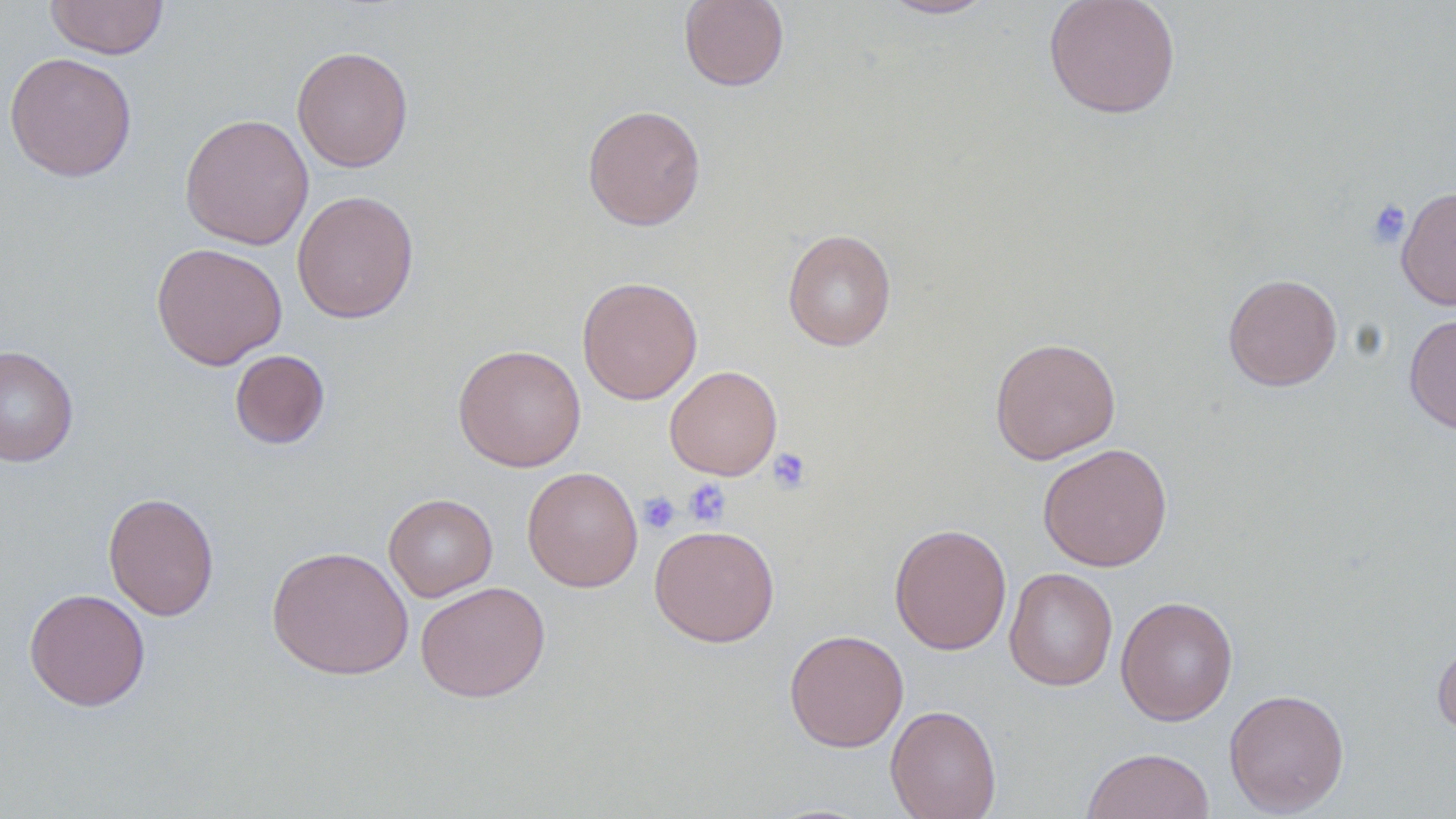

Summary:
  - Coordinate format: approximate bounding boxes as named x1/y1/x2/y2 corners in pixels
  - Platelet locations: (x1=1366, y1=198, x2=1411, y2=249), (x1=767, y1=447, x2=812, y2=494), (x1=682, y1=478, x2=731, y2=527), (x1=638, y1=491, x2=680, y2=534)
  - Uninfected red blood cell locations: (x1=45, y1=0, x2=169, y2=59), (x1=678, y1=0, x2=790, y2=91), (x1=878, y1=0, x2=997, y2=20), (x1=1043, y1=0, x2=1181, y2=118), (x1=292, y1=45, x2=414, y2=173), (x1=4, y1=52, x2=137, y2=182), (x1=582, y1=104, x2=706, y2=231), (x1=179, y1=112, x2=314, y2=250), (x1=1396, y1=185, x2=1456, y2=311), (x1=291, y1=190, x2=419, y2=324), (x1=783, y1=228, x2=897, y2=352), (x1=150, y1=242, x2=288, y2=370), (x1=1223, y1=272, x2=1342, y2=391), (x1=577, y1=276, x2=703, y2=404), (x1=1404, y1=312, x2=1456, y2=435), (x1=989, y1=336, x2=1121, y2=464), (x1=452, y1=343, x2=586, y2=472), (x1=0, y1=345, x2=78, y2=467), (x1=230, y1=349, x2=330, y2=449), (x1=664, y1=365, x2=782, y2=480), (x1=1037, y1=443, x2=1173, y2=571), (x1=522, y1=466, x2=643, y2=592), (x1=102, y1=492, x2=220, y2=621), (x1=384, y1=493, x2=498, y2=601), (x1=889, y1=523, x2=1012, y2=654), (x1=649, y1=524, x2=780, y2=648), (x1=266, y1=545, x2=414, y2=680), (x1=1004, y1=567, x2=1118, y2=691), (x1=415, y1=581, x2=550, y2=702), (x1=23, y1=588, x2=150, y2=711), (x1=1115, y1=595, x2=1238, y2=725), (x1=784, y1=629, x2=908, y2=752), (x1=1432, y1=639, x2=1456, y2=736), (x1=1224, y1=687, x2=1349, y2=816), (x1=885, y1=704, x2=1002, y2=819), (x1=1081, y1=747, x2=1216, y2=819)
  - Slide-level diagnosis: no evidence of blood parasites
  - Image size: 1456×819 pixels
  - Modality: optical microscopy
  - Stain: May-Grünwald-Giemsa
  - Field of view: single
  - Preparation: thin blood smear
  - Magnification: 1000x